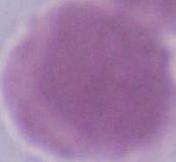

Summary:
  - Modality: photomicrograph
  - Identification: erythrocyte
  - Magnification: 1000x